Assess for malaria.
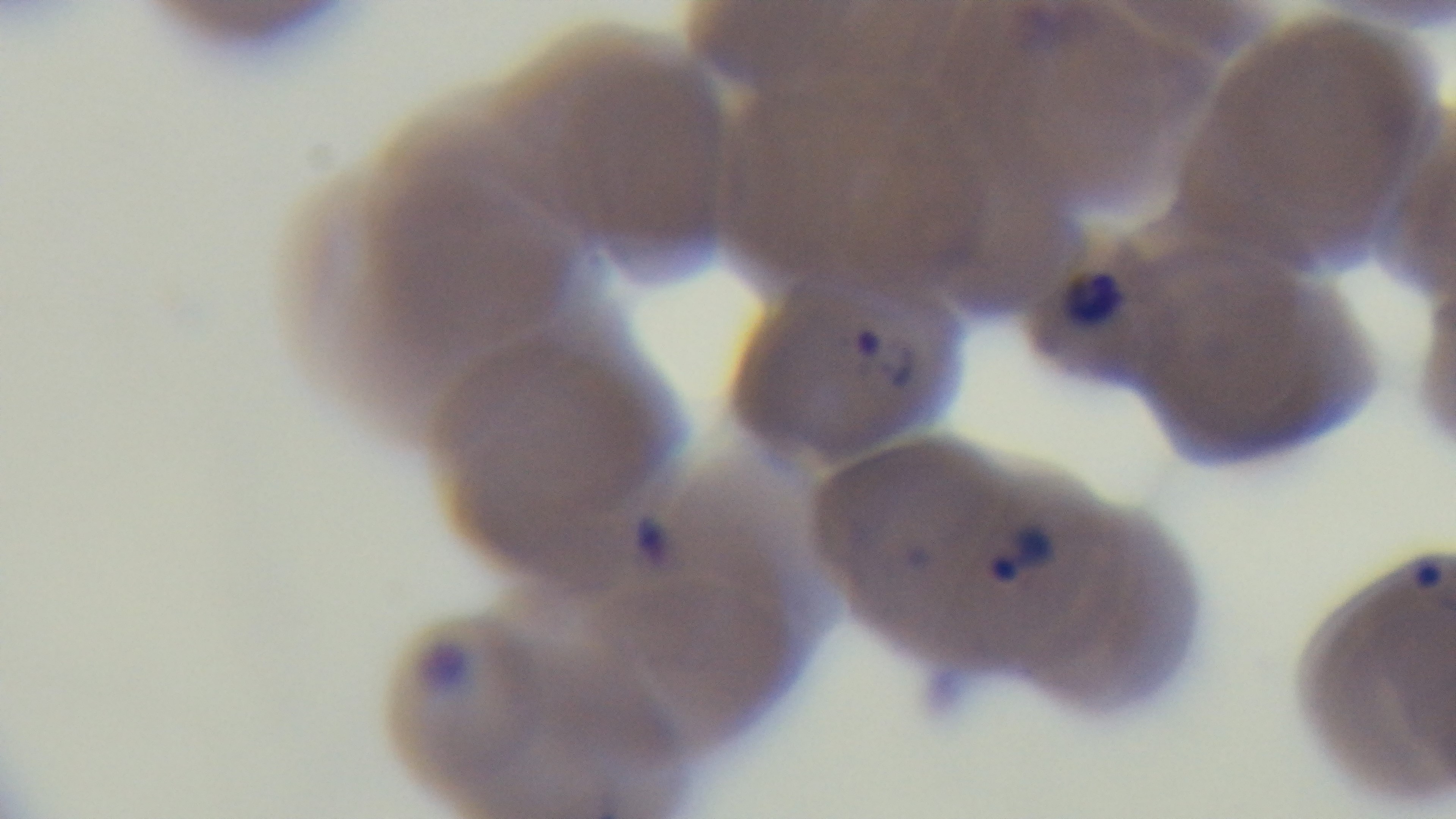

Positive.

Summary:
  - Stain: Giemsa
  - Capture: mounted 4K digital camera
  - Objective: 100x oil immersion
  - Preparation: thin
  - Field of view: single
  - Modality: light microscopy